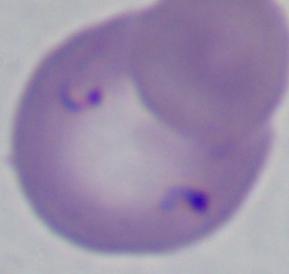 1000x magnification. Micrograph. A Babesia parasite is shown.